Classify this cell by malaria status.
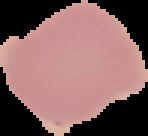

Uninfected.

Summary:
  - Preparation: thin blood smear
  - Image type: cell region segmented out of the field of view; surrounding area masked to black
  - Image size: 148×136 pixels